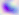 400x magnification. Toxoplasma gondii is seen. Micrograph.